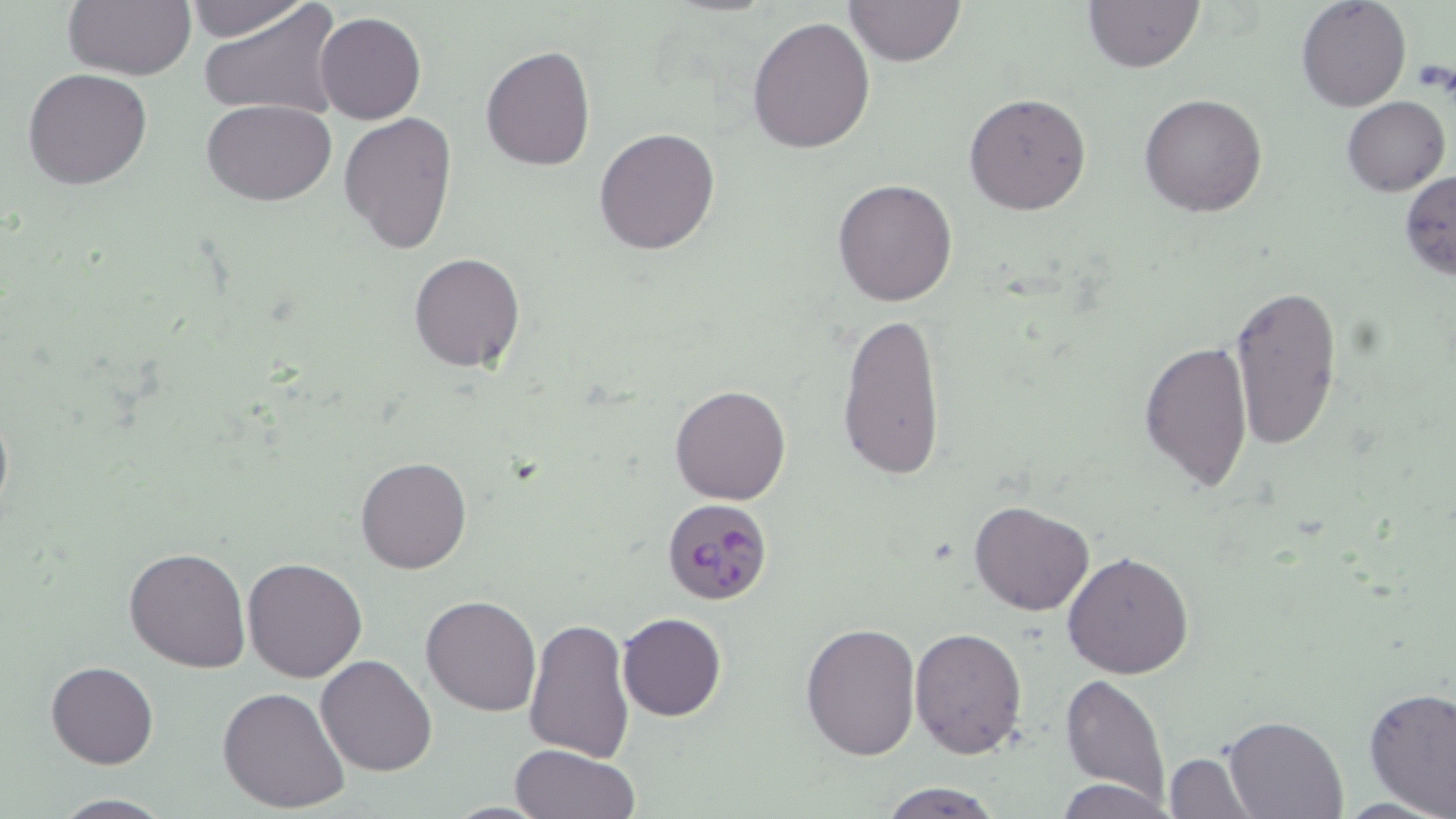

Approximate bounding boxes as [x1, y1, x2, y2] in pixels. Uninfected red blood cell locations: [182, 0, 315, 42], [846, 0, 965, 67], [1082, 0, 1203, 72], [1297, 0, 1411, 112], [62, 1, 196, 81], [199, 1, 345, 122], [314, 12, 426, 124], [747, 17, 877, 155], [480, 45, 597, 171], [23, 67, 152, 189], [963, 92, 1092, 214], [1140, 92, 1268, 216], [1342, 96, 1450, 195], [202, 99, 336, 203], [339, 112, 457, 256], [593, 127, 720, 255], [1399, 170, 1456, 280], [832, 177, 958, 306], [408, 252, 524, 372], [1229, 282, 1342, 453], [836, 311, 948, 481], [1138, 338, 1253, 494], [668, 384, 791, 506], [0, 395, 13, 531], [355, 455, 473, 574], [969, 500, 1094, 617], [124, 547, 251, 673], [1063, 551, 1195, 680], [242, 557, 367, 683], [421, 594, 541, 716], [616, 612, 727, 722], [521, 615, 635, 765], [801, 621, 922, 760], [910, 627, 1028, 758], [315, 654, 437, 776], [46, 660, 159, 769], [1060, 673, 1171, 804], [218, 686, 351, 812], [1362, 686, 1456, 816], [1224, 714, 1347, 818], [509, 743, 640, 819], [1163, 751, 1257, 818], [1053, 778, 1177, 818], [876, 779, 1005, 818], [48, 793, 176, 817]. Platelet locations: [1411, 59, 1456, 98]. Plasmodium falciparum-infected red blood cell locations: [661, 496, 772, 605]. Slide-level diagnosis: Plasmodium falciparum. May-Grünwald-Giemsa stain. Image is 1456×819 pixels. Light microscopy. One field of a larger specimen. 1000x magnification. Thin blood film.